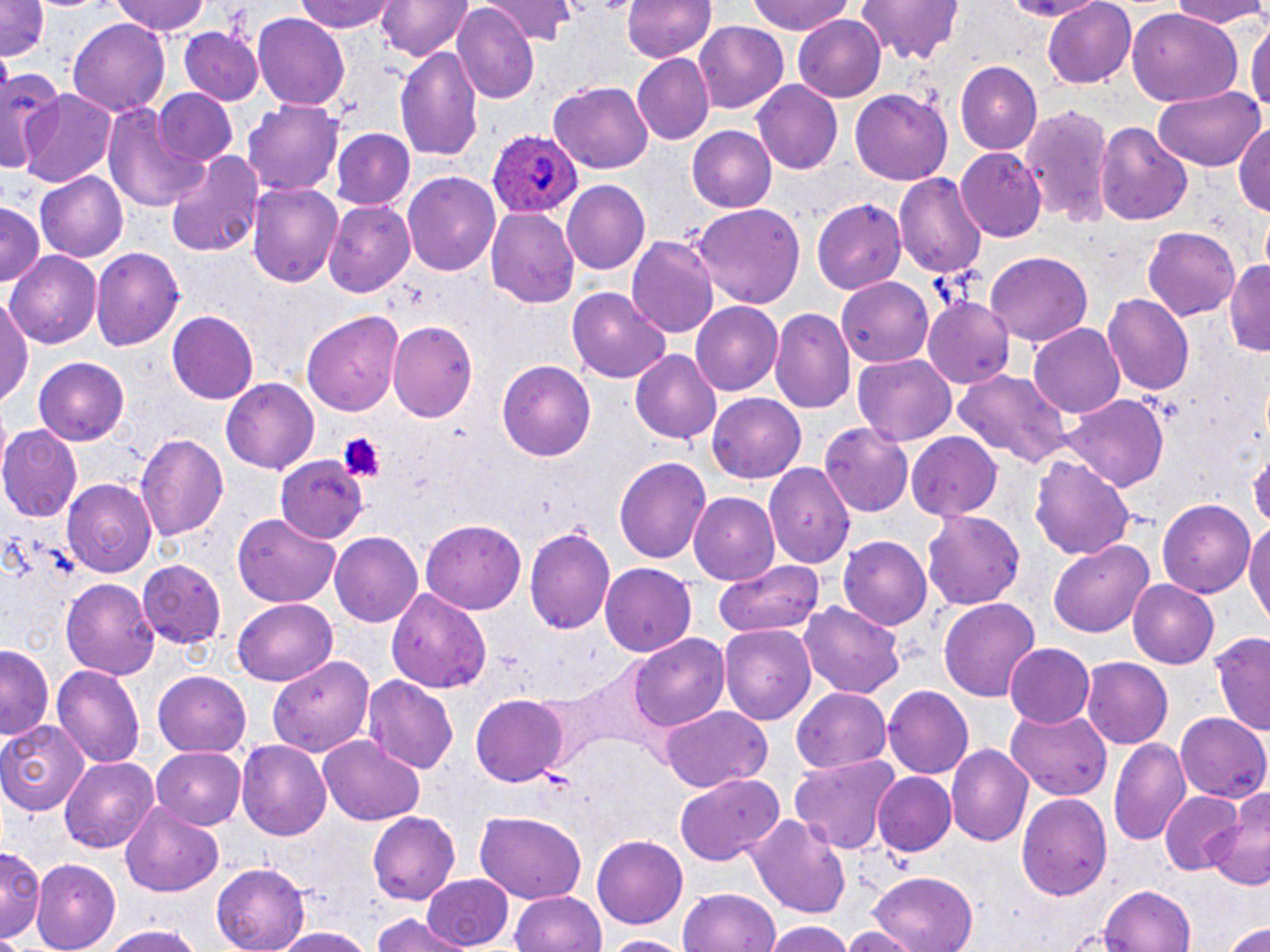
Plasmodium ovale-infected red blood cell locations = approximate bounding boxes as (x1, y1, x2, y2) in pixels: (487, 128, 580, 219)
slide-level diagnosis = Plasmodium ovale
modality = light microscopy
magnification = 1000x
image size = 1270×952 pixels
platelet locations = approximate bounding boxes as (x1, y1, x2, y2) in pixels: (336, 432, 382, 481)
preparation = thin blood smear
stain = May-Grünwald-Giemsa
uninfected red blood cell locations = approximate bounding boxes as (x1, y1, x2, y2) in pixels: (0, 0, 50, 62), (110, 0, 210, 37), (296, 0, 400, 34), (489, 0, 574, 45), (620, 0, 716, 64), (746, 0, 858, 35), (855, 0, 967, 66), (1040, 0, 1136, 88), (1163, 0, 1270, 30), (377, 1, 474, 64), (453, 6, 540, 105), (1128, 9, 1242, 109), (793, 14, 885, 102), (252, 15, 351, 109), (1247, 16, 1270, 132), (68, 17, 171, 118), (694, 23, 787, 112), (180, 27, 263, 106), (394, 45, 484, 164), (632, 55, 715, 145), (955, 62, 1042, 154), (0, 67, 65, 177), (550, 77, 653, 175), (753, 82, 844, 174), (1152, 85, 1264, 170), (16, 87, 118, 187), (154, 89, 239, 166), (852, 89, 950, 187), (243, 98, 345, 199), (102, 99, 210, 217), (1021, 105, 1114, 231), (1233, 119, 1270, 219), (1095, 121, 1194, 225), (686, 125, 776, 213), (331, 130, 416, 210), (957, 148, 1045, 242), (163, 151, 265, 261), (35, 169, 126, 262), (402, 172, 501, 275), (894, 172, 986, 279), (246, 180, 344, 291), (562, 181, 650, 275), (813, 196, 911, 293), (324, 202, 415, 298), (0, 204, 44, 290), (692, 205, 806, 310), (485, 207, 580, 308), (1143, 227, 1239, 320), (629, 233, 719, 338), (91, 247, 183, 352), (8, 250, 101, 349), (984, 253, 1092, 349), (1225, 257, 1270, 359), (836, 275, 935, 367), (568, 288, 672, 383), (1103, 294, 1194, 397), (926, 295, 1014, 389), (1, 296, 32, 409), (690, 299, 784, 393), (771, 306, 856, 417), (301, 310, 403, 416), (167, 312, 259, 406), (388, 319, 479, 422), (1028, 323, 1128, 418), (630, 350, 721, 444), (854, 354, 958, 446), (34, 356, 131, 445), (498, 361, 595, 462), (951, 368, 1076, 467), (222, 380, 319, 472), (707, 393, 806, 484), (1066, 395, 1169, 493), (821, 423, 912, 516), (0, 426, 82, 522), (136, 432, 230, 547), (905, 432, 1004, 523), (1249, 450, 1270, 530), (275, 454, 368, 544), (614, 456, 713, 562), (1031, 456, 1132, 563), (764, 463, 856, 568), (62, 478, 160, 578), (689, 492, 781, 584), (1157, 498, 1259, 599), (923, 511, 1026, 609), (1245, 512, 1270, 629), (234, 514, 338, 609), (420, 518, 525, 613), (526, 525, 617, 638), (329, 532, 424, 627), (840, 537, 931, 631), (1048, 541, 1154, 638), (712, 558, 823, 642), (136, 561, 226, 649), (601, 564, 697, 655), (60, 578, 162, 680), (1127, 578, 1222, 668), (389, 587, 492, 694), (936, 597, 1041, 702), (233, 599, 336, 687), (800, 603, 906, 698), (721, 623, 815, 725), (1207, 631, 1270, 740), (630, 636, 728, 733), (1006, 644, 1095, 729), (1, 648, 54, 741), (269, 655, 375, 756), (1083, 657, 1172, 750), (53, 664, 144, 771), (153, 671, 250, 757), (364, 675, 459, 774), (884, 686, 973, 778), (790, 688, 893, 774), (470, 693, 568, 788), (661, 706, 770, 793), (1007, 706, 1115, 800), (1174, 712, 1270, 802), (0, 718, 91, 813), (320, 736, 424, 823), (1109, 736, 1192, 847), (235, 738, 332, 840), (947, 743, 1033, 846), (152, 748, 245, 827), (790, 755, 900, 853), (61, 756, 159, 853), (871, 771, 956, 857), (674, 772, 785, 868), (1209, 785, 1270, 890), (1017, 791, 1112, 899), (1159, 791, 1245, 875), (120, 803, 225, 897), (368, 810, 460, 904), (473, 810, 589, 902), (750, 810, 853, 922), (593, 836, 687, 929), (0, 846, 43, 942), (31, 860, 121, 950), (212, 864, 308, 952), (865, 870, 979, 952), (421, 873, 516, 947), (1098, 885, 1199, 952), (679, 887, 780, 952), (510, 889, 607, 952), (371, 913, 471, 952), (1223, 917, 1270, 951), (761, 920, 855, 952), (844, 921, 917, 952), (98, 924, 206, 952), (269, 926, 379, 952), (603, 934, 689, 951)
field of view = single